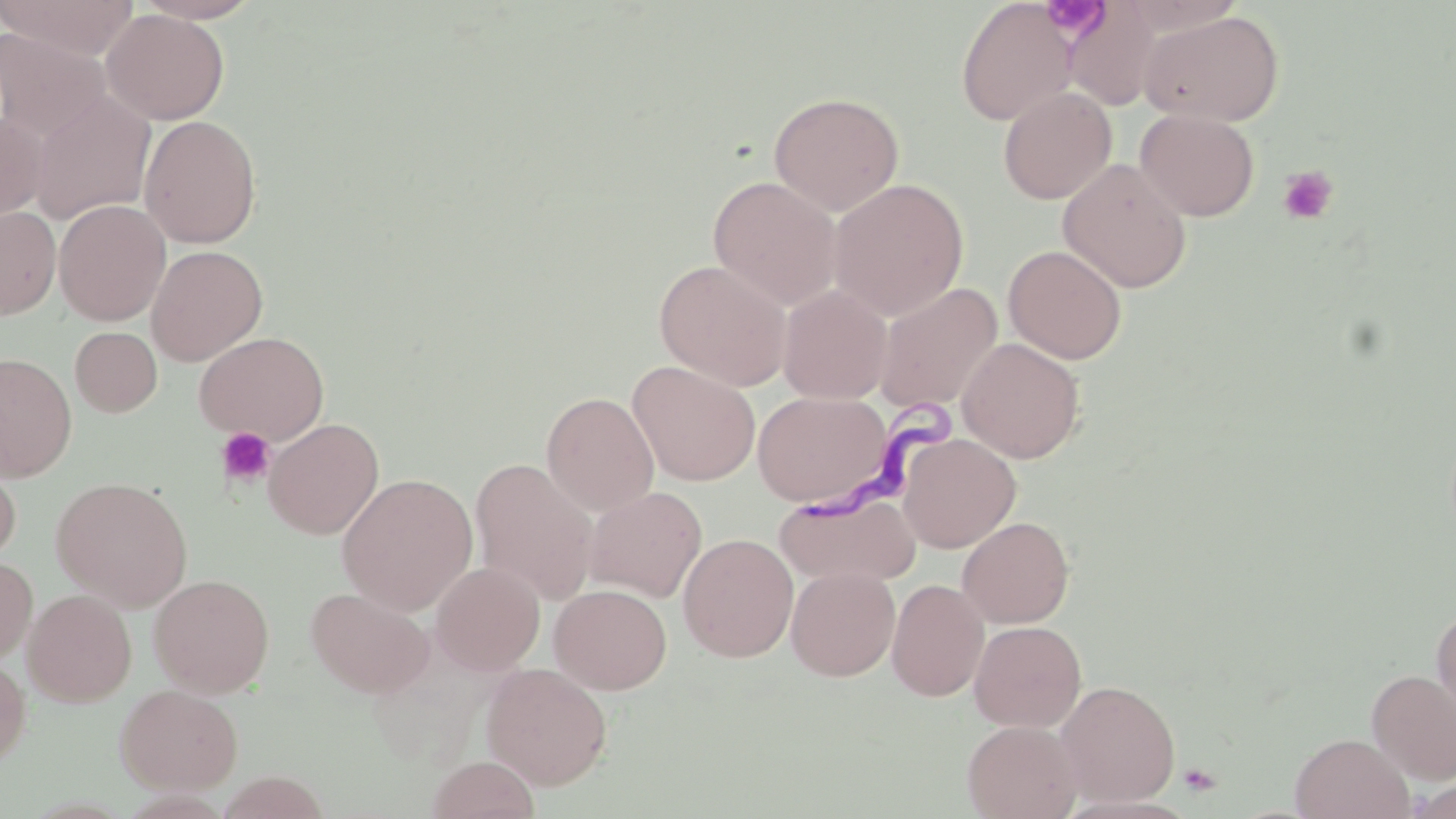
slide_level_diagnosis: Trypanosoma brucei
field_of_view: one of a larger specimen
magnification: 1000x
platelet_locations: 'approximate bounding boxes as [x1, y1, x2, y2] in pixels: [1040, 1, 1107, 38], [1277, 166, 1339, 225], [216, 427, 276, 488], [1178, 762, 1223, 797]'
preparation: thin blood smear
trypanosoma_brucei_locations: 'approximate bounding boxes as [x1, y1, x2, y2] in pixels: [804, 388, 968, 529]'
stain: May-Grünwald-Giemsa
uninfected_red_blood_cell_locations: 'approximate bounding boxes as [x1, y1, x2, y2] in pixels: [0, 0, 140, 60], [133, 0, 265, 24], [955, 1, 1077, 126], [1061, 1, 1171, 111], [101, 8, 229, 125], [1139, 10, 1285, 127], [0, 28, 110, 143], [997, 87, 1117, 204], [28, 89, 156, 226], [768, 91, 904, 215], [1135, 109, 1260, 221], [0, 110, 48, 225], [138, 115, 262, 249], [1058, 158, 1193, 294], [708, 175, 843, 310], [829, 178, 969, 321], [53, 199, 171, 326], [0, 206, 61, 319], [1002, 244, 1127, 364], [146, 245, 267, 366], [655, 258, 792, 391], [874, 282, 1003, 414], [778, 285, 893, 404], [70, 327, 162, 417], [194, 331, 329, 445], [957, 338, 1085, 463], [0, 353, 77, 481], [627, 360, 761, 486], [752, 390, 895, 509], [541, 391, 659, 515], [263, 417, 384, 539], [898, 433, 1021, 553], [0, 455, 21, 567], [470, 457, 599, 605], [336, 473, 478, 616], [51, 476, 193, 611], [584, 486, 707, 603], [775, 492, 921, 587], [957, 516, 1075, 628], [678, 533, 799, 662], [0, 557, 37, 663], [430, 562, 545, 676], [786, 566, 900, 681], [149, 573, 275, 697], [887, 578, 989, 701], [549, 584, 672, 695], [305, 586, 435, 698], [23, 589, 137, 707], [1431, 605, 1456, 721], [969, 620, 1086, 732], [0, 657, 31, 768], [481, 662, 612, 790], [1367, 670, 1456, 784], [1054, 680, 1181, 806], [115, 684, 244, 795], [962, 720, 1083, 819], [1290, 732, 1414, 819], [427, 755, 539, 819], [216, 771, 330, 818]'
modality: light microscopy
image_size: 1456×819 pixels